Name the cell type shown.
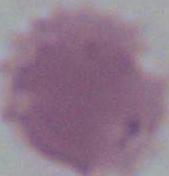
An erythrocyte.

Micrograph. Captured at 1000x magnification.